State the blood parasite species.
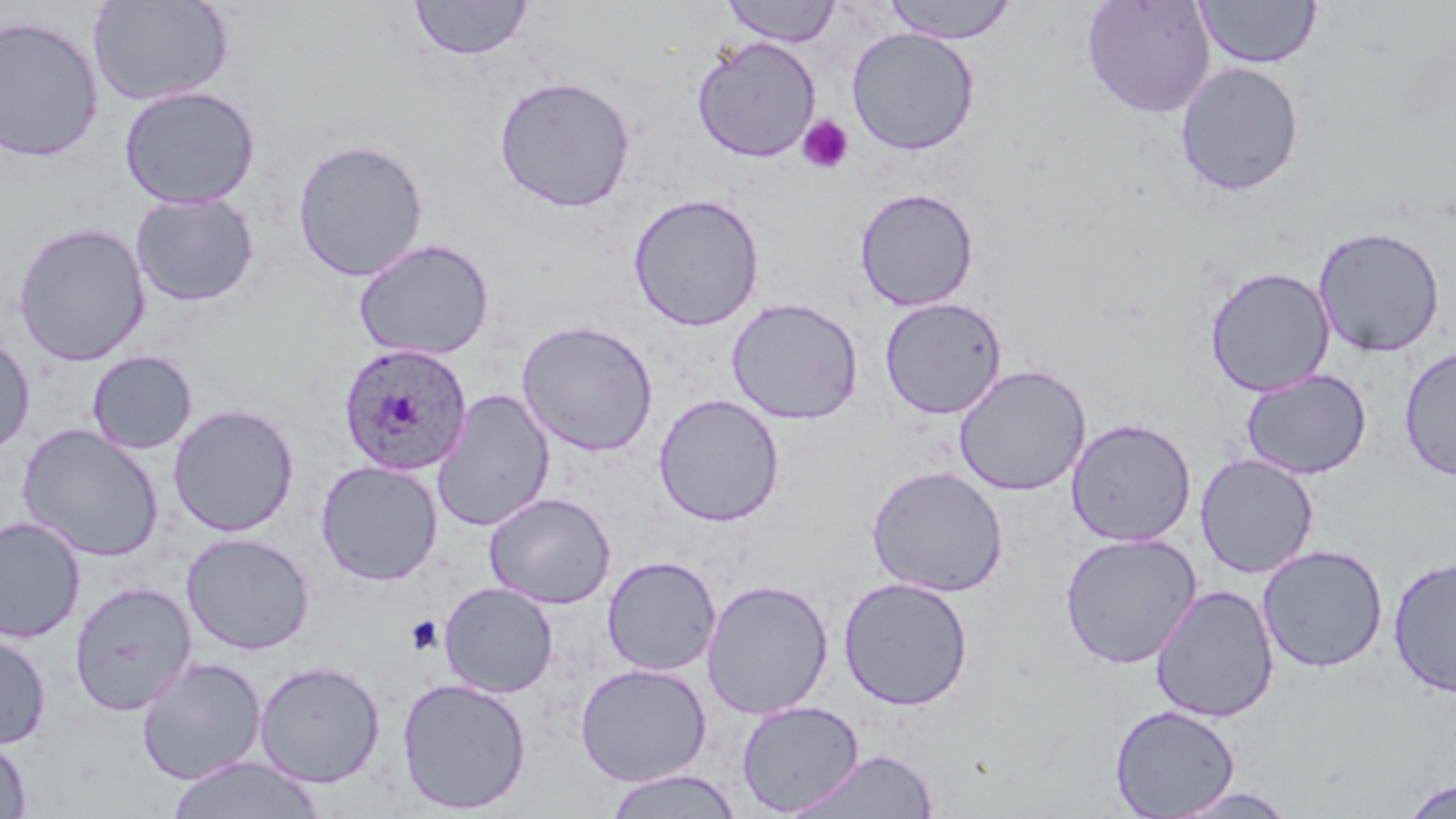
Plasmodium ovale.

uninfected red blood cell locations = approximate bounding boxes as (x1,y1)-(x2,y2) corner pairs in pixels: (722,0)-(841,46), (884,0)-(1017,44), (1081,0)-(1216,119), (1195,0)-(1322,69), (88,1)-(234,106), (409,1)-(532,61), (0,14)-(105,162), (846,26)-(980,156), (692,35)-(821,162), (1174,61)-(1305,197), (494,75)-(635,212), (119,85)-(261,210), (291,138)-(429,281), (854,187)-(979,311), (628,192)-(765,331), (130,193)-(259,307), (13,222)-(150,366), (1312,225)-(1446,358), (353,237)-(495,361), (1204,266)-(1336,396), (878,296)-(1007,420), (726,297)-(863,425), (516,319)-(659,457), (0,331)-(36,456), (1399,346)-(1456,482), (86,350)-(198,454), (952,363)-(1091,496), (1240,369)-(1371,479), (431,389)-(556,531), (654,393)-(785,527), (167,404)-(300,537), (1067,417)-(1196,547), (16,424)-(165,562), (1195,454)-(1319,579), (316,460)-(443,586), (866,465)-(1008,597), (485,492)-(616,609), (0,516)-(86,643), (181,532)-(315,655), (1059,532)-(1202,669), (1257,544)-(1388,673), (602,556)-(721,676), (1387,557)-(1456,698), (838,577)-(974,711), (701,579)-(833,719), (69,582)-(197,716), (439,582)-(559,698), (1150,584)-(1279,722), (0,629)-(51,750), (136,656)-(267,786), (253,661)-(385,787), (574,662)-(712,787), (396,676)-(532,814), (736,700)-(864,815), (1110,704)-(1241,818), (0,733)-(32,818), (787,749)-(939,818), (166,755)-(326,819), (603,769)-(742,819), (1399,776)-(1455,818), (1168,786)-(1300,818)
magnification = 1000x
preparation = thin blood film
image size = 1456×819 pixels
field of view = single
platelet locations = approximate bounding boxes as (x1,y1)-(x2,y2) corner pairs in pixels: (796,114)-(854,175), (405,615)-(442,655)
Plasmodium ovale-infected red blood cell locations = approximate bounding boxes as (x1,y1)-(x2,y2) corner pairs in pixels: (337,343)-(474,476)
stain = May-Grünwald-Giemsa
modality = light microscopy